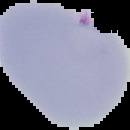

{
  "image_size": "130×130 pixels",
  "preparation": "thin blood film",
  "malaria_status": "parasitized",
  "image_type": "segmented cell region with the area outside set to black"
}